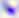

modality = photomicrograph
identification = Toxoplasma gondii
magnification = 400x